Describe the morphology of the red blood cells.
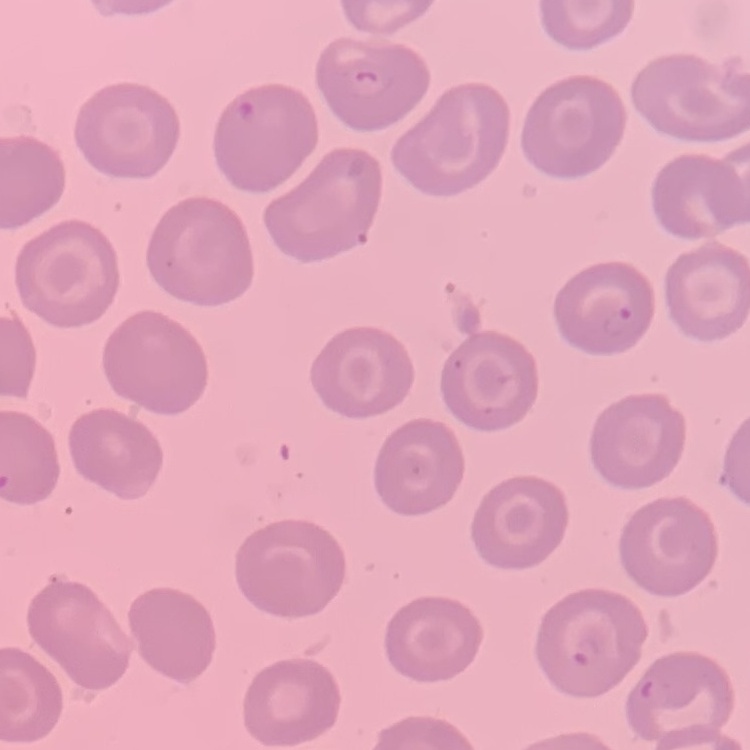
No rouleaux formation.

stain = Field's or Giemsa
preparation = thin blood smear
image type = one tile cut from a larger photomicrograph